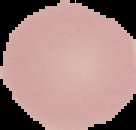
result = negative for malaria parasites
image size = 136×130 pixels
image type = segmented cell region with the area outside set to black
preparation = thin blood smear